Locate every uninfected red blood cell.
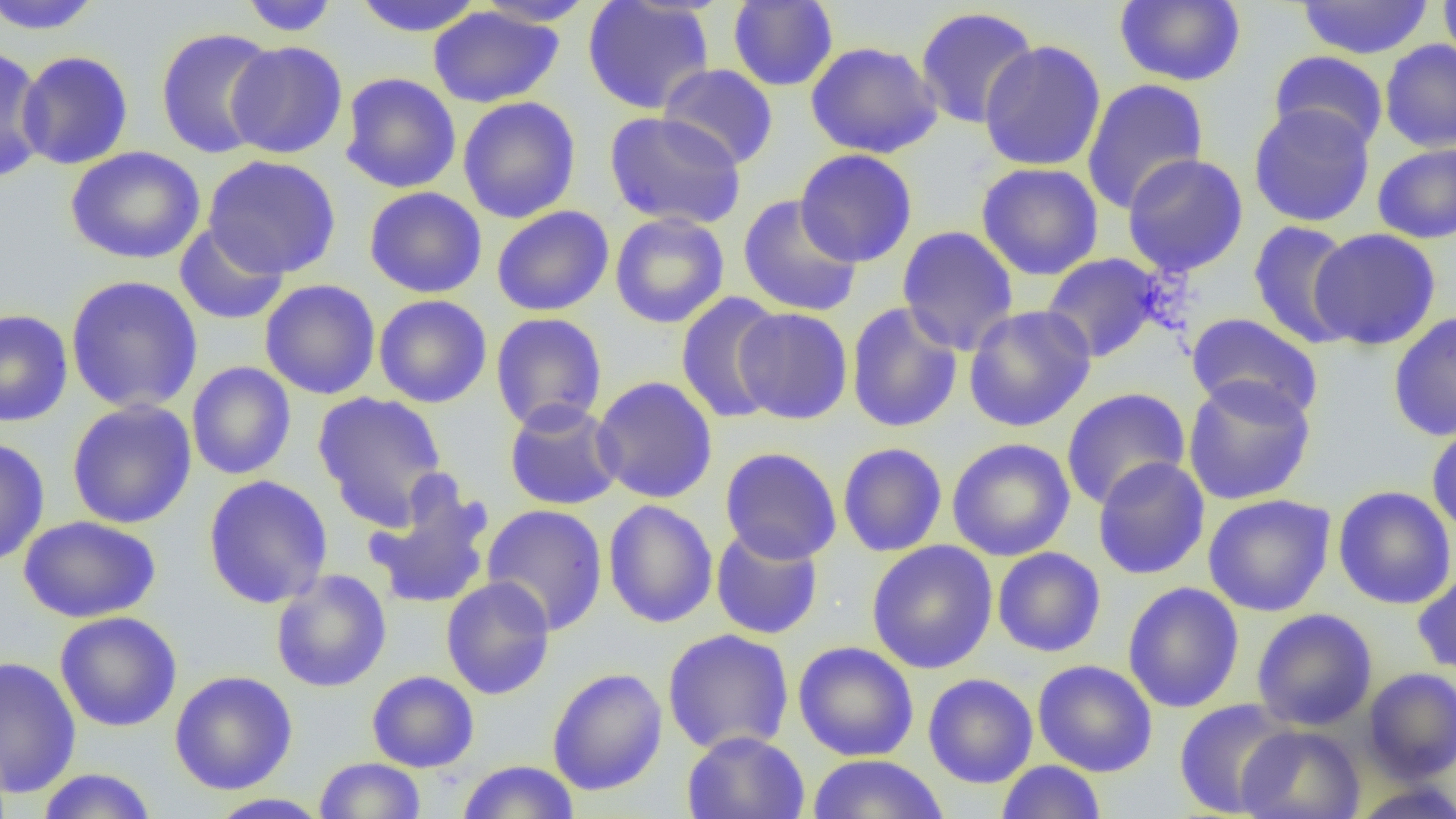
Approximate bounding boxes as (x1, y1, x2, y2) in pixels.
Uninfected red blood cells: (0, 0, 107, 35), (238, 0, 340, 35), (352, 0, 485, 37), (582, 0, 715, 115), (1113, 0, 1247, 87), (1438, 0, 1456, 70), (473, 1, 597, 27), (728, 1, 839, 91), (1296, 1, 1434, 59), (428, 6, 564, 108), (914, 6, 1040, 130), (155, 27, 279, 159), (1379, 39, 1456, 153), (978, 40, 1107, 171), (225, 41, 348, 159), (806, 41, 942, 159), (0, 46, 49, 184), (1269, 50, 1388, 152), (16, 51, 133, 170), (658, 63, 778, 170), (339, 72, 461, 193), (1082, 77, 1209, 215), (457, 96, 581, 223), (1248, 104, 1376, 227), (603, 110, 747, 229), (1372, 143, 1456, 244), (65, 146, 205, 265), (795, 149, 918, 268), (1122, 153, 1248, 277), (202, 155, 341, 279), (976, 161, 1104, 281), (364, 186, 487, 298), (738, 195, 863, 317), (491, 205, 614, 316), (610, 212, 730, 328), (1247, 220, 1360, 349), (174, 222, 290, 326), (896, 225, 1019, 355), (1308, 228, 1441, 351), (1040, 253, 1164, 363), (65, 275, 204, 414), (259, 279, 381, 400), (675, 291, 787, 425), (374, 294, 492, 408), (846, 302, 963, 433), (964, 304, 1096, 432), (734, 307, 853, 424), (0, 309, 73, 427), (1388, 310, 1456, 442), (490, 312, 607, 432), (1185, 312, 1324, 423), (186, 361, 296, 480), (591, 376, 718, 504), (1183, 376, 1315, 506), (1061, 387, 1191, 510), (312, 391, 449, 530), (66, 399, 197, 529), (503, 400, 624, 510), (1426, 422, 1456, 537), (946, 437, 1075, 561), (0, 438, 50, 568), (837, 442, 948, 557), (720, 446, 842, 564), (1092, 456, 1210, 580), (203, 475, 334, 609), (363, 479, 495, 611), (1332, 485, 1456, 610), (1203, 493, 1336, 617), (603, 500, 718, 628), (481, 504, 608, 635), (18, 515, 160, 623), (711, 525, 824, 639), (866, 540, 998, 674), (992, 547, 1106, 657), (270, 569, 392, 692), (1412, 571, 1456, 677), (441, 576, 555, 700), (1122, 581, 1245, 713), (1251, 608, 1378, 731), (54, 611, 183, 732), (662, 628, 795, 755), (793, 641, 920, 760), (0, 655, 82, 798), (1032, 659, 1158, 777), (547, 667, 668, 796), (1362, 667, 1456, 783), (169, 670, 298, 795), (366, 670, 479, 772), (923, 672, 1038, 788), (1173, 698, 1300, 817), (1236, 725, 1366, 819), (681, 730, 810, 819), (807, 754, 949, 818), (314, 757, 427, 818), (456, 759, 580, 818), (996, 760, 1106, 819), (35, 768, 158, 819), (1349, 780, 1456, 819), (206, 793, 333, 818).

slide-level diagnosis = no evidence of blood parasites
preparation = thin blood film
magnification = 1000x
modality = optical microscopy
image size = 1456×819 pixels
field of view = single